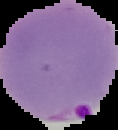
image type = segmented cell region on a black background
image size = 118×130 pixels
result = malaria parasites detected
preparation = thin blood smear